Assess the morphology of the erythrocytes.
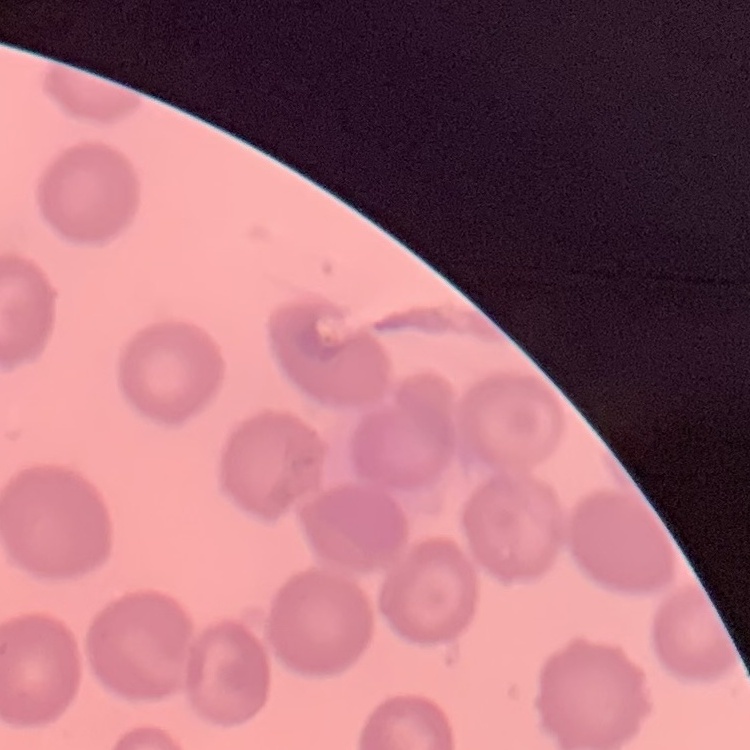
No rouleaux formation.

image type = square crop of a larger photomicrograph
preparation = thin blood smear
stain = Field's or Giemsa